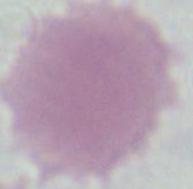

Photomicrograph. A red blood cell is shown. 1000x magnification.